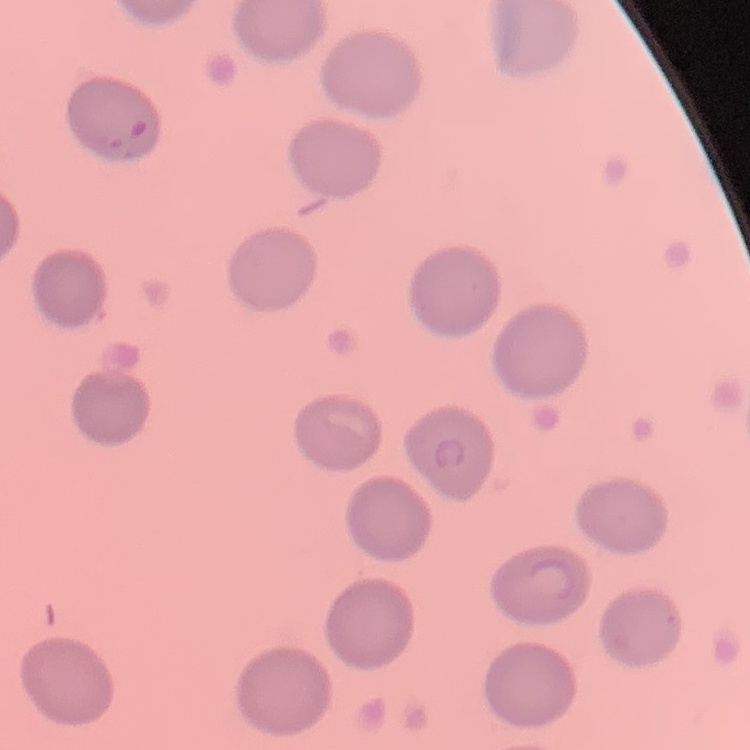

erythrocyte morphology = no rouleaux formation
image type = one tile cut from a larger photomicrograph
stain = Field's or Giemsa
preparation = thin peripheral smear